Locate every blood parasite and identify its species.
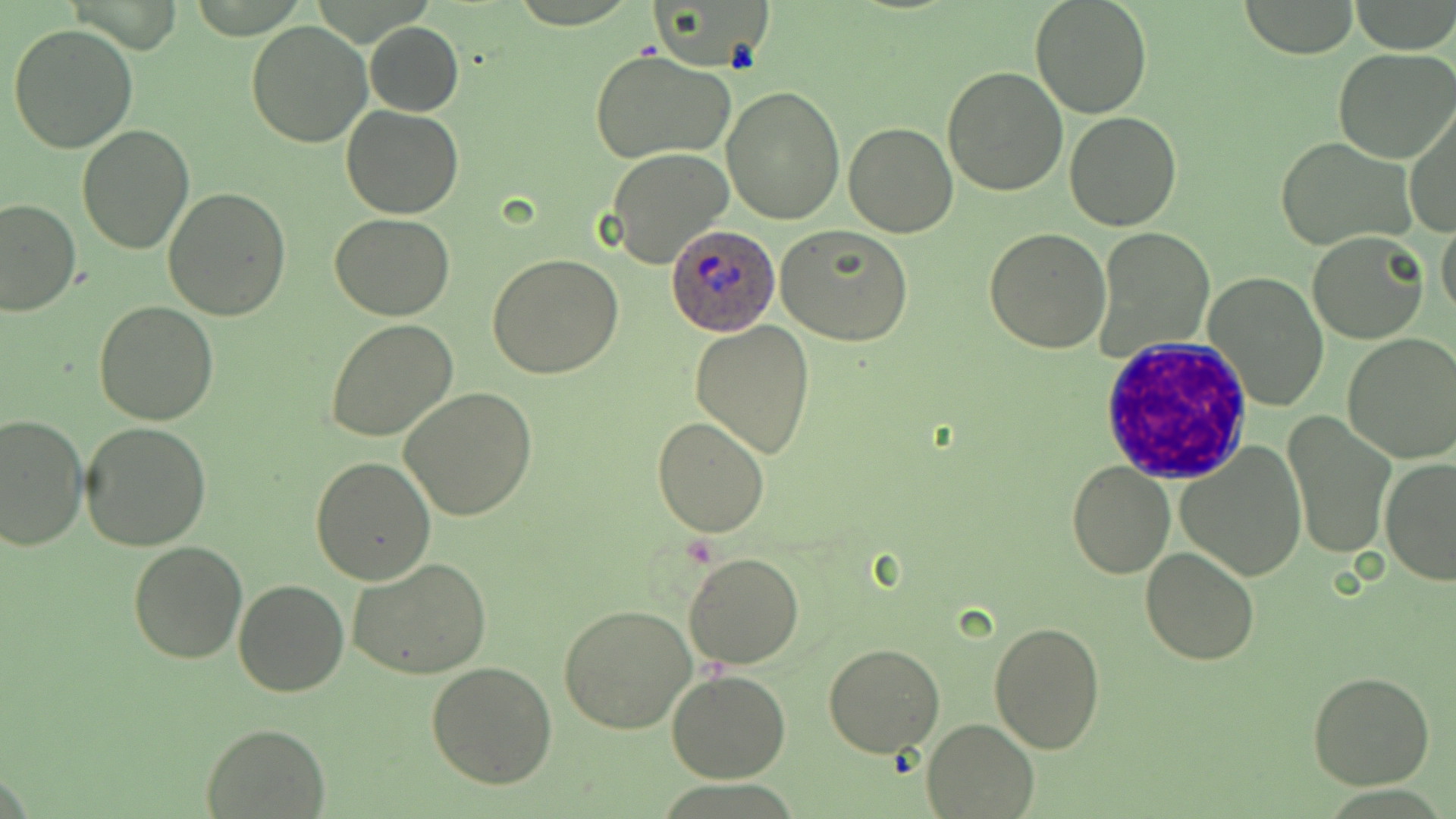

Approximate bounding boxes as (x1,y1)-(x2,y2) corner pairs in pixels.
Plasmodium ovale-infected red blood cells: (667,222)-(780,336).
No Plasmodium falciparum, Plasmodium malariae, Plasmodium vivax, Babesia divergens, or Trypanosoma brucei observed.

slide-level diagnosis = Plasmodium ovale
image size = 1456×819 pixels
magnification = 1000x
uninfected red blood cell locations = approximate bounding boxes as (x1,y1)-(x2,y2) corner pairs in pixels: (655,0)-(772,70), (1028,0)-(1153,119), (1234,1)-(1360,57), (246,20)-(372,148), (366,22)-(463,116), (7,23)-(139,155), (1334,48)-(1456,163), (589,49)-(735,165), (942,66)-(1070,196), (722,86)-(844,224), (1405,103)-(1456,240), (341,105)-(465,219), (1065,109)-(1182,230), (843,122)-(958,238), (76,126)-(194,254), (1276,139)-(1415,249), (605,146)-(733,269), (163,187)-(291,320), (0,197)-(79,317), (331,214)-(455,322), (1436,218)-(1456,324), (777,226)-(916,348), (983,228)-(1111,354), (1096,228)-(1213,360), (1308,231)-(1430,344), (489,252)-(624,378), (1203,272)-(1330,410), (94,301)-(218,425), (325,319)-(459,442), (690,319)-(816,459), (1340,333)-(1456,463), (398,386)-(537,522), (0,412)-(88,551), (1283,413)-(1396,560), (651,415)-(773,537), (79,420)-(213,553), (1176,439)-(1308,580), (310,456)-(437,587), (1380,457)-(1456,586), (1067,461)-(1175,581), (128,539)-(248,664), (1138,546)-(1260,666), (684,553)-(804,670), (348,558)-(493,679), (234,579)-(349,696), (558,604)-(699,735), (987,622)-(1107,753), (824,642)-(945,757), (427,661)-(558,788), (666,670)-(792,783), (1307,671)-(1436,790), (921,717)-(1038,818), (200,723)-(329,817)
white blood cell locations = approximate bounding boxes as (x1,y1)-(x2,y2) corner pairs in pixels: (1099,336)-(1251,484)
preparation = thin blood smear
modality = light microscopy
stain = May-Grünwald-Giemsa
field of view = single